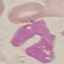
Summary:
  - Malaria status: uninfected
  - Image type: automatically extracted cell patch, resized to 64 × 64 pixels
  - Stain: Giemsa
  - Capture: smartphone camera at the microscope eyepiece
  - Preparation: thin smear